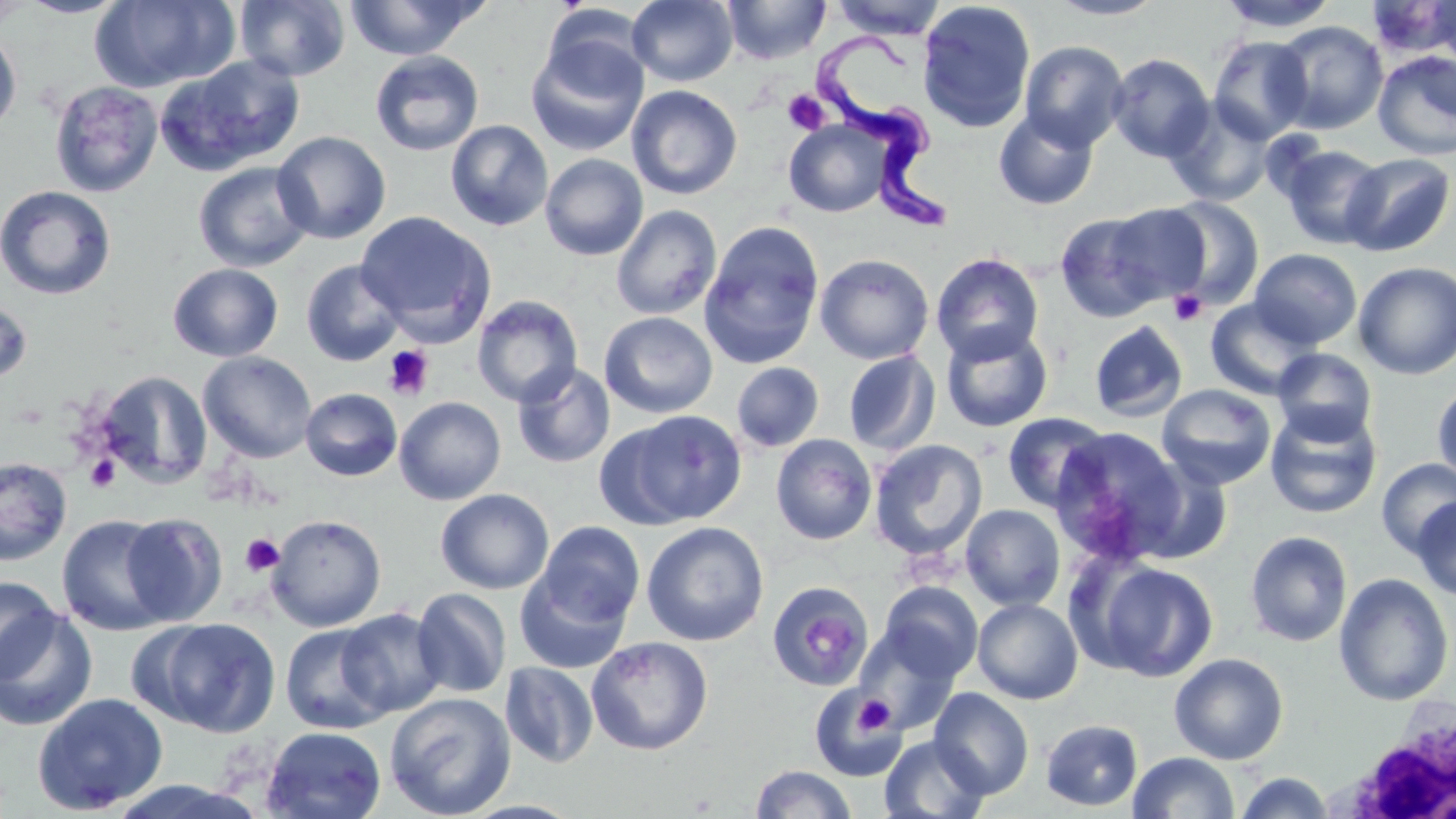
Approximate bounding boxes as [x1, y1, x2, y2] in pixels. Platelet locations: [783, 90, 830, 135], [1169, 290, 1208, 326], [383, 345, 435, 401], [85, 455, 121, 494], [240, 533, 285, 577], [855, 695, 894, 733]. Trypanosoma brucei locations: [814, 31, 965, 235]. Uninfected red blood cell locations: [0, 0, 37, 25], [15, 0, 133, 18], [90, 0, 235, 93], [235, 0, 350, 81], [345, 0, 486, 61], [627, 0, 738, 86], [724, 0, 830, 64], [830, 0, 947, 39], [1045, 0, 1167, 20], [1216, 0, 1339, 32], [1425, 0, 1456, 68], [917, 1, 1036, 133], [1369, 1, 1455, 60], [541, 4, 653, 93], [1272, 20, 1388, 134], [0, 27, 22, 139], [1208, 35, 1314, 144], [527, 40, 648, 156], [1019, 40, 1129, 151], [370, 51, 484, 156], [1372, 51, 1456, 161], [1107, 53, 1215, 163], [163, 54, 307, 173], [49, 80, 163, 197], [627, 84, 743, 200], [1165, 98, 1277, 208], [993, 108, 1099, 210], [445, 120, 553, 232], [784, 120, 893, 218], [272, 131, 391, 244], [1279, 144, 1386, 249], [540, 153, 648, 260], [1341, 153, 1455, 256], [193, 161, 315, 272], [0, 185, 117, 300], [1158, 196, 1265, 310], [1102, 203, 1213, 304], [611, 205, 722, 320], [356, 211, 497, 342], [1054, 212, 1169, 324], [699, 220, 825, 369], [1249, 248, 1363, 349], [930, 252, 1045, 364], [814, 253, 934, 365], [300, 259, 406, 366], [168, 262, 283, 362], [1353, 262, 1456, 379], [471, 295, 584, 407], [0, 298, 34, 385], [1204, 299, 1318, 400], [599, 311, 718, 418], [1089, 320, 1189, 423], [940, 323, 1054, 433], [1272, 348, 1377, 445], [198, 351, 317, 463], [843, 351, 941, 456], [512, 361, 615, 469], [731, 361, 824, 452], [95, 370, 212, 489], [1432, 381, 1456, 487], [1157, 384, 1276, 490], [300, 387, 402, 481], [394, 396, 506, 505], [1264, 406, 1382, 519], [608, 409, 748, 528], [1001, 413, 1112, 513], [1049, 426, 1187, 564], [771, 434, 877, 545], [869, 438, 988, 560], [0, 457, 73, 565], [1127, 457, 1234, 565], [1376, 458, 1456, 558], [436, 489, 554, 595], [1411, 498, 1456, 600], [960, 504, 1066, 610], [120, 512, 228, 627], [57, 514, 173, 636], [266, 514, 387, 632], [536, 521, 645, 628], [641, 521, 769, 646], [1245, 531, 1352, 647], [1091, 560, 1219, 682], [514, 569, 631, 674], [1334, 573, 1454, 706], [0, 574, 60, 682], [767, 581, 873, 691], [879, 582, 983, 683], [411, 588, 512, 698], [972, 598, 1083, 704], [0, 608, 99, 731], [336, 608, 447, 718], [143, 617, 282, 737], [280, 622, 394, 734], [853, 627, 962, 736], [586, 636, 713, 755], [1169, 652, 1289, 765], [500, 661, 598, 768], [809, 687, 908, 782], [930, 688, 1033, 799], [32, 692, 168, 815], [384, 692, 516, 818], [1041, 719, 1143, 811], [261, 726, 386, 818], [879, 735, 990, 819], [1128, 752, 1240, 818], [750, 765, 856, 819], [1235, 771, 1334, 818], [102, 780, 268, 817]. White blood cell locations: [1355, 718, 1456, 819]. Slide-level diagnosis: Trypanosoma brucei. Single field of view. May-Grünwald-Giemsa stain. Light microscopy. Thin blood smear. Image is 1456×819 pixels. Captured at 1000x magnification.